Identify the cell.
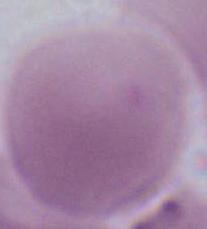
An erythrocyte.

Summary:
  - Modality: photomicrograph
  - Magnification: 1000x